Identify the blood parasite species.
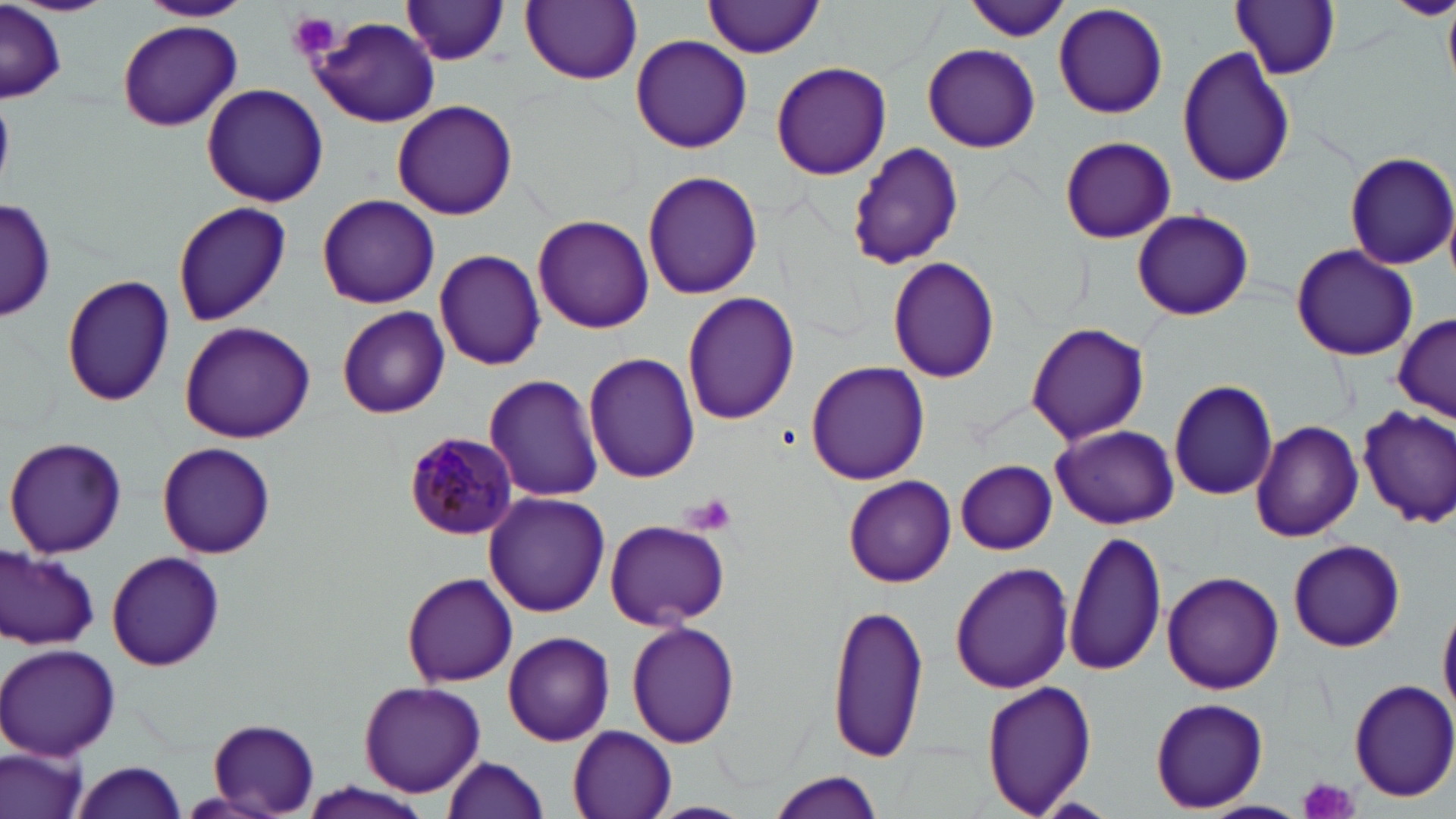

Plasmodium malariae.

Summary:
  - Coordinate format: approximate bounding boxes as (x1,y1)-(x2,y2) corner pairs in pixels
  - Plasmodium malariae-infected red blood cell locations: (405,432)-(519,543)
  - Uninfected red blood cell locations: (138,0)-(252,24), (703,0)-(826,58), (1229,0)-(1340,80), (1388,0)-(1456,20), (402,1)-(511,65), (521,1)-(643,84), (964,1)-(1071,43), (0,3)-(64,103), (1053,3)-(1169,119), (1443,4)-(1455,90), (305,15)-(442,127), (118,21)-(241,131), (630,34)-(753,154), (922,42)-(1041,154), (1178,46)-(1297,187), (771,60)-(891,180), (201,83)-(329,207), (392,99)-(518,220), (1059,136)-(1176,245), (848,143)-(965,268), (1344,151)-(1456,270), (641,170)-(763,301), (315,194)-(439,309), (0,198)-(56,321), (171,202)-(291,325), (1133,208)-(1253,321), (532,213)-(654,333), (1289,245)-(1418,360), (433,248)-(545,369), (886,256)-(1001,384), (60,275)-(175,407), (680,291)-(801,427), (336,306)-(448,418), (1394,314)-(1455,422), (178,321)-(315,443), (1024,322)-(1152,446), (585,352)-(701,484), (806,358)-(930,485), (483,373)-(604,501), (1168,378)-(1279,502), (1356,403)-(1456,528), (1250,420)-(1363,542), (1050,424)-(1178,529), (5,435)-(127,558), (157,441)-(276,558), (955,460)-(1058,555), (843,476)-(956,585), (484,491)-(610,617), (604,519)-(731,630), (1062,528)-(1166,677), (1288,538)-(1405,653), (0,546)-(100,650), (106,550)-(225,671), (950,562)-(1073,693), (1163,572)-(1284,694), (402,573)-(517,687), (1438,594)-(1456,726), (828,600)-(930,765), (626,621)-(738,748), (503,631)-(615,746), (1,644)-(121,759), (1350,678)-(1456,802), (359,680)-(486,798), (980,681)-(1098,816), (1149,697)-(1268,813), (207,719)-(323,815), (566,724)-(679,819), (2,743)-(91,819), (441,754)-(551,818), (69,758)-(191,819), (766,770)-(886,818), (298,781)-(431,819), (646,801)-(755,819)
  - Platelet locations: (286,11)-(341,61), (681,492)-(738,535), (1296,775)-(1360,819)
  - Stain: May-Grünwald-Giemsa
  - Field of view: single
  - Image size: 1456×819 pixels
  - Modality: optical microscopy
  - Preparation: thin blood film
  - Magnification: 1000x